Point out each leukocyte.
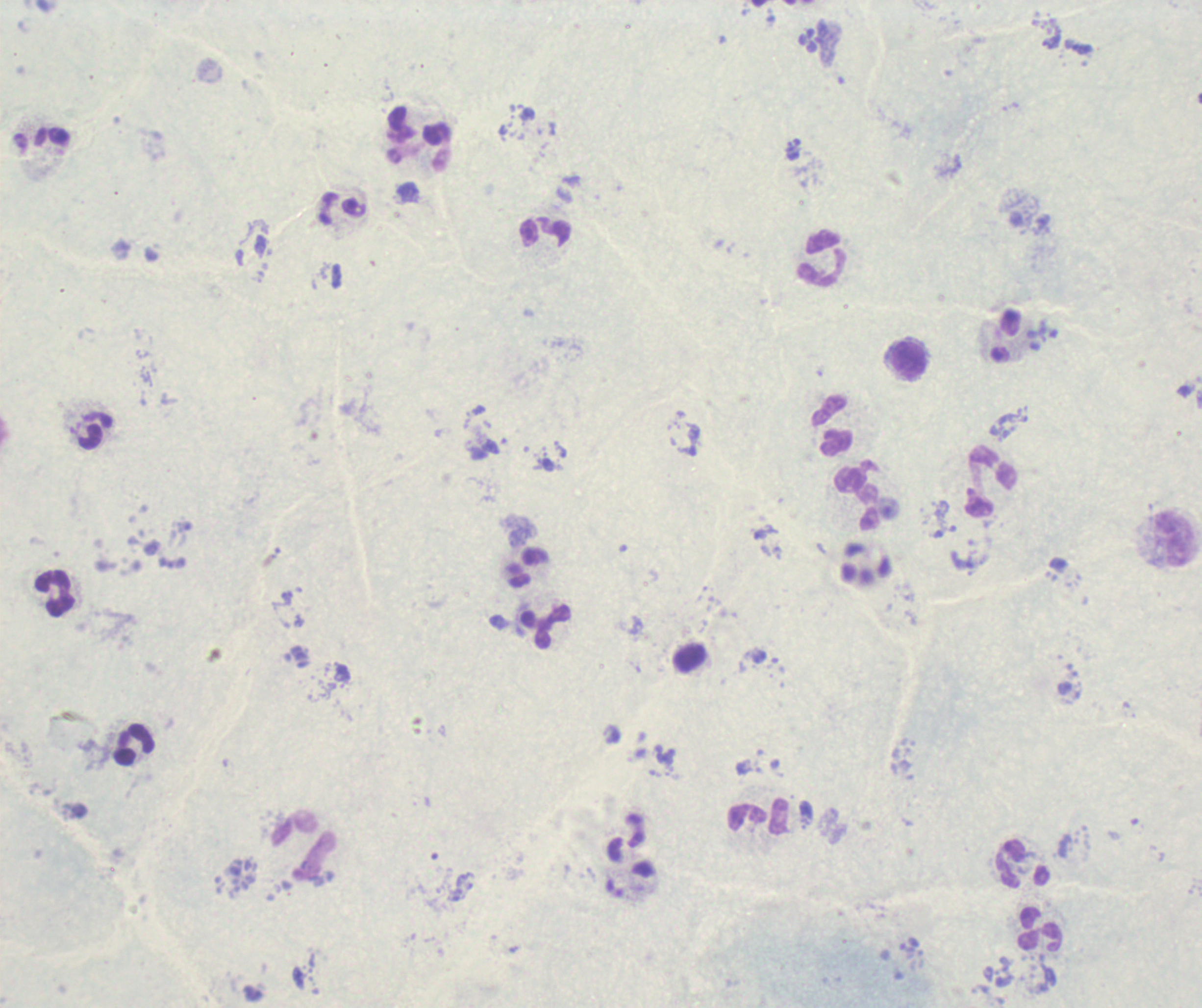
Approximate centers as [x, y] in pixels.
Leukocytes: [544, 232], [824, 258], [910, 361], [832, 425], [991, 482], [858, 499], [1175, 540], [528, 568], [55, 594], [545, 627], [136, 743], [757, 817], [305, 846], [1023, 864], [1040, 929].

{
  "background_quality": "unsatisfactory",
  "field_of_view": "one from this slide",
  "image_size": "1202×1008 pixels",
  "context": "previously used in an actual diagnosis",
  "magnification": "100x",
  "trophozoite_locations": "approximate centers as [x, y] in pixels: [793, 150]",
  "stain": "Romanowsky",
  "result": "malaria parasites detected",
  "preparation": "thick smear of blood"
}